Report the malaria status of this cell.
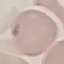
Uninfected.

Cell patch, automatically extracted from a larger field of view and resized to 64 × 64 pixels. Thin blood smear. Giemsa-stained preparation. Photographed with a smartphone camera at the microscope eyepiece.